Find each WBC.
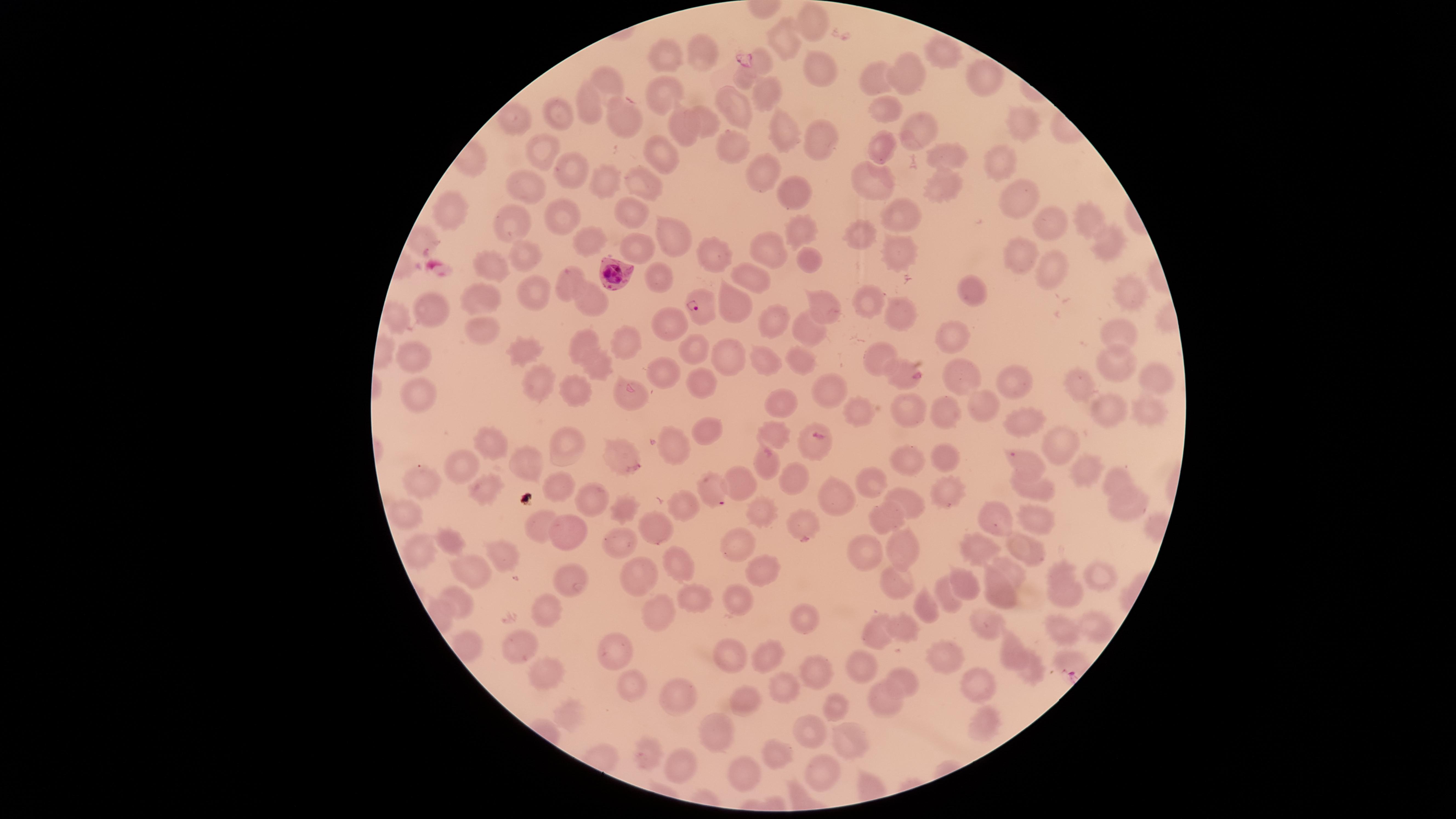

No WBCs identified.

Approximate marker points as (x, y) in pixels.
Summary:
  - Uninfected RBCs: (808, 20), (782, 39), (946, 46), (665, 56), (702, 57), (758, 62), (813, 71), (908, 74), (985, 75), (877, 76), (743, 77), (613, 82), (764, 93), (663, 97), (885, 105), (735, 106), (590, 108), (563, 113), (705, 121), (626, 123), (1019, 124), (681, 126), (783, 127), (915, 131), (818, 136), (734, 143), (878, 145), (660, 149), (539, 150), (957, 155), (1001, 164), (565, 166), (764, 171), (609, 175), (646, 178), (871, 178), (528, 183), (793, 185), (940, 186), (1021, 194), (627, 209), (901, 209), (449, 211), (562, 217), (1085, 222), (513, 223), (1042, 223), (666, 227), (801, 228), (860, 234), (587, 238), (1101, 239), (768, 241), (638, 245), (711, 249), (523, 250), (897, 253), (1020, 253), (813, 259), (496, 268), (1055, 268), (655, 272), (745, 277), (567, 280), (531, 288), (1127, 289), (972, 293), (487, 296), (595, 296), (731, 296), (868, 302), (822, 304), (427, 312), (899, 314), (773, 323), (669, 327), (481, 330), (805, 331), (955, 331), (1117, 336), (631, 338), (587, 341), (528, 344), (695, 348), (416, 352), (876, 352), (730, 354), (760, 357), (1112, 360), (805, 363), (600, 366), (1154, 372), (962, 373), (899, 374), (663, 375), (1012, 375), (1083, 378), (541, 381), (708, 382), (828, 386), (626, 387), (423, 389), (572, 391), (786, 403), (984, 405), (1106, 407), (908, 409), (856, 410), (1025, 410), (948, 414), (1154, 419), (704, 429), (776, 433), (564, 441), (814, 442), (1055, 443), (497, 444), (620, 445), (674, 449), (942, 458), (528, 459), (1022, 462), (462, 463), (764, 463), (904, 463), (1085, 474), (795, 476), (427, 477), (872, 477), (740, 479), (1119, 481), (709, 485), (483, 486), (560, 486), (1024, 488), (947, 491), (587, 494), (830, 495), (907, 499), (995, 505), (1118, 505), (686, 508), (759, 508), (628, 509), (402, 512), (881, 513), (1042, 517), (799, 525), (538, 526), (650, 526), (452, 538), (563, 538), (618, 540), (901, 541), (975, 542), (734, 544), (420, 548), (1018, 548), (506, 552), (863, 555), (675, 558), (768, 565), (1011, 567), (1058, 570), (475, 571), (641, 572), (563, 574), (1100, 575), (966, 578), (899, 581), (999, 582), (945, 592), (1064, 592), (739, 594), (460, 596), (693, 598), (543, 607), (924, 607), (660, 610), (798, 620), (987, 622), (1094, 624), (901, 626), (1062, 629), (873, 630), (1013, 645), (513, 646), (945, 647), (614, 650), (770, 650), (731, 654), (548, 667), (1029, 669), (861, 670), (820, 671), (626, 679), (904, 681), (979, 685), (669, 686), (783, 686), (742, 699), (886, 700), (832, 706), (569, 711), (984, 722), (813, 727), (719, 729), (852, 740), (646, 753), (777, 754), (680, 762), (825, 766), (748, 773)
  - Parasitized RBCs: (609, 270), (698, 308)
  - Preparation: thin smear of blood
  - Stain: Giemsa
  - Capture: smartphone photograph through the microscope eyepiece
  - Presence: malaria parasites detected
  - Species: Plasmodium falciparum
  - Field of view: single
  - Image size: 1456×819 pixels
  - Visible region: circular